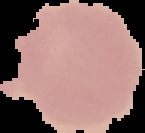
result: no malaria parasites detected
image_size: 145×133 pixels
image_type: cell region segmented out of the field of view; surrounding area masked to black
preparation: thin blood smear